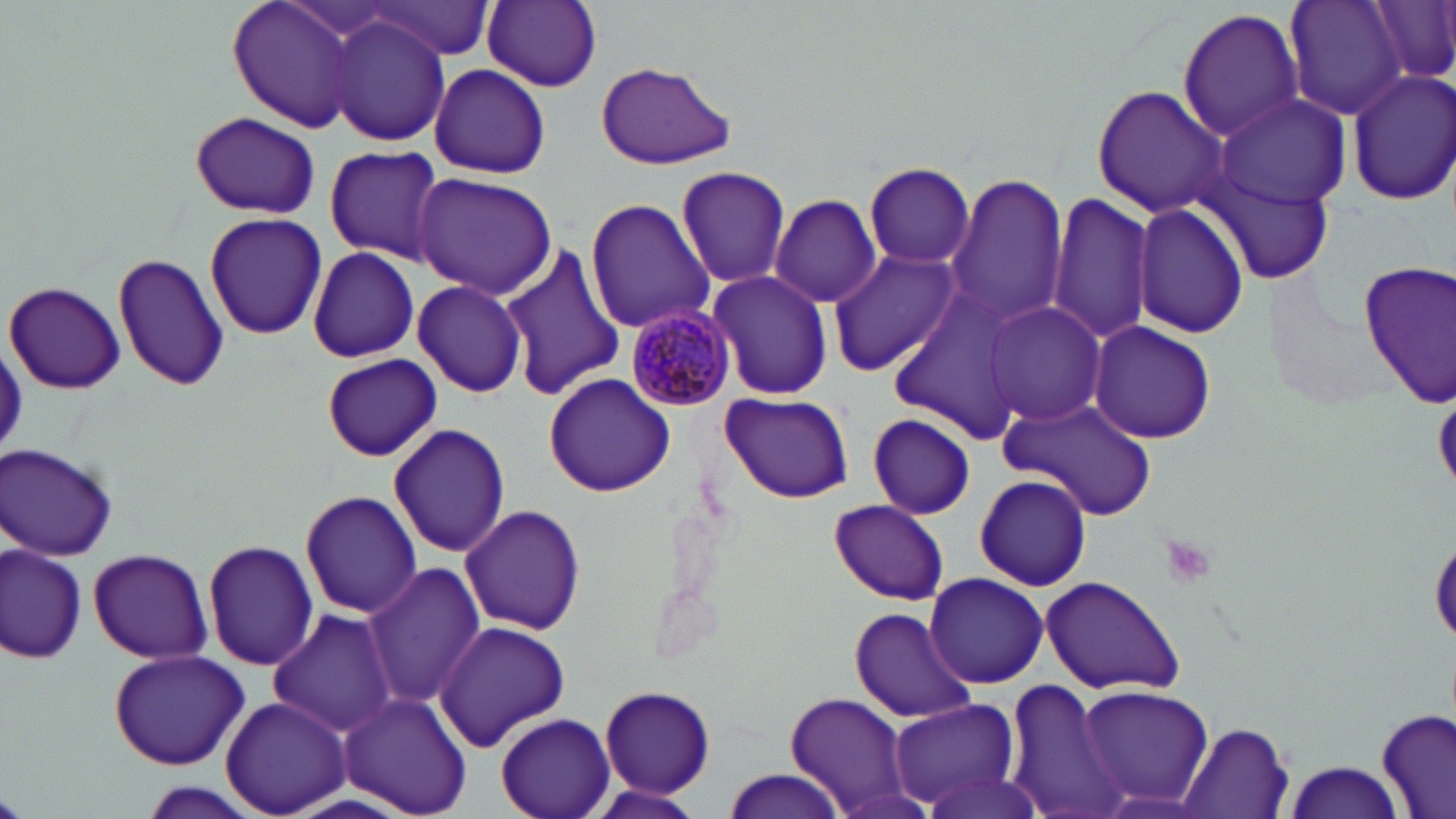
slide-level diagnosis = Plasmodium malariae
image size = 1456×819 pixels
uninfected red blood cell locations = approximate bounding boxes as (x1, y1, x2, y2) in pixels: (227, 0, 370, 135), (361, 0, 493, 62), (481, 0, 603, 90), (1282, 0, 1412, 120), (1370, 0, 1456, 85), (1177, 8, 1305, 143), (327, 15, 450, 147), (593, 62, 734, 170), (429, 64, 550, 178), (1346, 68, 1456, 205), (1090, 85, 1225, 216), (1213, 93, 1353, 208), (190, 111, 322, 220), (323, 144, 446, 264), (865, 161, 975, 269), (675, 167, 791, 288), (413, 172, 555, 298), (945, 174, 1068, 325), (1047, 192, 1158, 345), (770, 194, 881, 308), (585, 197, 713, 333), (1132, 204, 1249, 338), (204, 211, 328, 340), (499, 243, 624, 402), (307, 245, 422, 364), (826, 249, 961, 376), (113, 250, 229, 394), (1358, 259, 1455, 406), (706, 270, 833, 401), (5, 281, 125, 395), (412, 281, 527, 395), (886, 292, 1029, 433), (980, 301, 1106, 427), (1088, 321, 1216, 445), (322, 354, 442, 461), (544, 374, 674, 496), (720, 391, 852, 503), (999, 397, 1158, 520), (864, 413, 980, 521), (389, 424, 512, 559), (2, 443, 121, 561), (973, 473, 1091, 590), (297, 487, 423, 620), (829, 501, 950, 605), (459, 503, 589, 636), (1430, 530, 1456, 647), (203, 539, 320, 670), (2, 542, 88, 667), (88, 547, 213, 664), (361, 563, 486, 710), (922, 572, 1050, 689), (1037, 575, 1186, 696), (267, 608, 401, 737), (850, 609, 979, 724), (431, 619, 570, 753), (108, 648, 252, 771), (1001, 675, 1128, 819), (1077, 683, 1214, 811), (597, 684, 717, 798), (336, 690, 472, 817), (785, 691, 912, 816), (220, 694, 351, 818), (887, 698, 1021, 815), (1377, 708, 1454, 819), (495, 711, 615, 819), (1177, 722, 1293, 819), (1283, 760, 1405, 819), (913, 767, 1047, 819), (719, 769, 849, 818)
modality = optical microscopy
platelet locations = approximate bounding boxes as (x1, y1, x2, y2) in pixels: (1159, 536, 1216, 591)
preparation = thin blood smear
field of view = one of a larger specimen
Plasmodium malariae-infected red blood cell locations = approximate bounding boxes as (x1, y1, x2, y2) in pixels: (624, 304, 735, 412)
magnification = 1000x
stain = May-Grünwald-Giemsa